Report the malaria status of this cell.
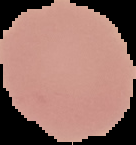

It is uninfected.

image size = 136×145 pixels
image type = segmented cell region with the area outside set to black
preparation = thin blood film